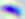

Summary:
  - Modality: photomicrograph
  - Magnification: 400x
  - Identification: Toxoplasma gondii